Give the extent of all Plasmodium falciparum-infected red blood cells.
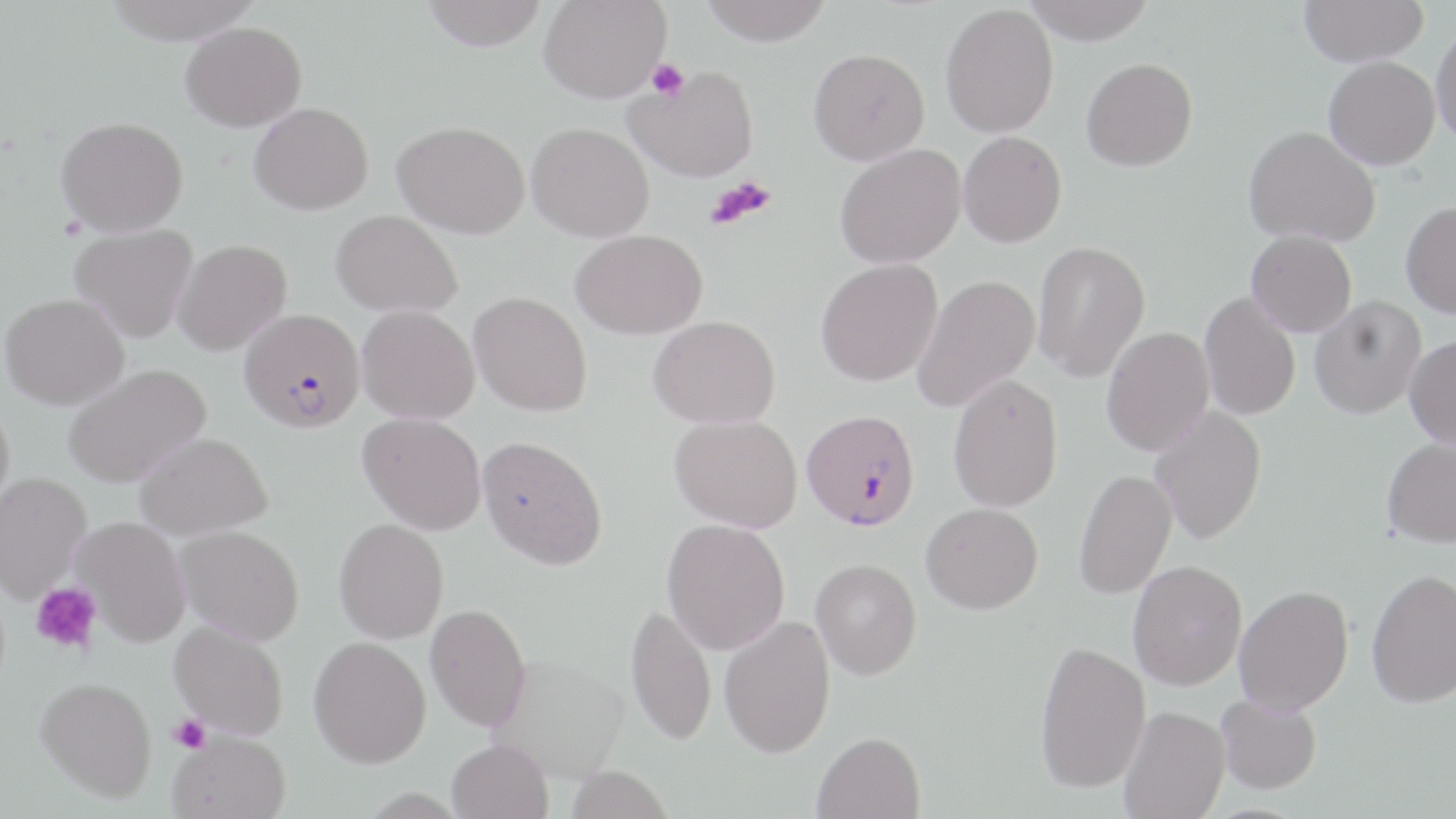

Approximate bounding boxes as named x1/y1/x2/y2 corners in pixels.
Plasmodium falciparum-infected red blood cells: (x1=239, y1=308, x2=366, y2=433), (x1=801, y1=408, x2=921, y2=531).

slide-level diagnosis = Plasmodium falciparum
preparation = thin blood film
magnification = 1000x
modality = optical microscopy
field of view = one of a larger specimen
stain = May-Grünwald-Giemsa
platelet locations = approximate bounding boxes as named x1/y1/x2/y2 corners in pixels: (x1=645, y1=59, x2=689, y2=100), (x1=707, y1=176, x2=777, y2=229), (x1=30, y1=582, x2=103, y2=655), (x1=168, y1=714, x2=211, y2=753)
image size = 1456×819 pixels
uninfected red blood cell locations = approximate bounding boxes as named x1/y1/x2/y2 corners in pixels: (x1=100, y1=0, x2=265, y2=44), (x1=420, y1=0, x2=549, y2=51), (x1=539, y1=0, x2=671, y2=102), (x1=699, y1=0, x2=833, y2=46), (x1=1021, y1=0, x2=1157, y2=44), (x1=1298, y1=0, x2=1428, y2=66), (x1=940, y1=3, x2=1059, y2=138), (x1=181, y1=21, x2=306, y2=131), (x1=1431, y1=21, x2=1456, y2=147), (x1=808, y1=48, x2=930, y2=165), (x1=1323, y1=56, x2=1440, y2=170), (x1=1081, y1=58, x2=1197, y2=171), (x1=626, y1=66, x2=759, y2=182), (x1=249, y1=102, x2=373, y2=215), (x1=56, y1=116, x2=188, y2=236), (x1=392, y1=121, x2=530, y2=239), (x1=526, y1=123, x2=654, y2=242), (x1=1243, y1=125, x2=1380, y2=246), (x1=958, y1=131, x2=1067, y2=247), (x1=834, y1=143, x2=966, y2=269), (x1=1401, y1=201, x2=1456, y2=318), (x1=331, y1=210, x2=462, y2=316), (x1=69, y1=223, x2=199, y2=342), (x1=570, y1=229, x2=708, y2=339), (x1=1246, y1=230, x2=1357, y2=337), (x1=172, y1=239, x2=291, y2=355), (x1=1032, y1=239, x2=1151, y2=383), (x1=815, y1=258, x2=942, y2=387), (x1=912, y1=274, x2=1040, y2=413), (x1=468, y1=291, x2=592, y2=416), (x1=1199, y1=291, x2=1301, y2=421), (x1=1, y1=293, x2=129, y2=410), (x1=1310, y1=296, x2=1426, y2=419), (x1=357, y1=305, x2=479, y2=423), (x1=648, y1=315, x2=781, y2=428), (x1=1101, y1=326, x2=1215, y2=457), (x1=1403, y1=334, x2=1456, y2=449), (x1=62, y1=363, x2=211, y2=488), (x1=948, y1=373, x2=1063, y2=512), (x1=0, y1=397, x2=15, y2=520), (x1=1148, y1=405, x2=1267, y2=546), (x1=358, y1=412, x2=487, y2=535), (x1=669, y1=414, x2=802, y2=532), (x1=134, y1=432, x2=273, y2=539), (x1=477, y1=434, x2=608, y2=570), (x1=1381, y1=435, x2=1456, y2=548), (x1=1073, y1=468, x2=1177, y2=600), (x1=0, y1=472, x2=90, y2=602), (x1=920, y1=503, x2=1043, y2=614), (x1=73, y1=516, x2=190, y2=646), (x1=333, y1=518, x2=448, y2=643), (x1=661, y1=518, x2=791, y2=654), (x1=175, y1=525, x2=304, y2=645), (x1=811, y1=559, x2=922, y2=680), (x1=1128, y1=560, x2=1247, y2=690), (x1=1366, y1=568, x2=1456, y2=707), (x1=1234, y1=585, x2=1353, y2=715), (x1=625, y1=601, x2=717, y2=746), (x1=426, y1=603, x2=531, y2=731), (x1=719, y1=616, x2=835, y2=758), (x1=170, y1=621, x2=289, y2=740), (x1=309, y1=635, x2=431, y2=768), (x1=1034, y1=639, x2=1150, y2=794), (x1=488, y1=654, x2=630, y2=780), (x1=36, y1=677, x2=157, y2=801), (x1=1216, y1=694, x2=1321, y2=794), (x1=1119, y1=706, x2=1230, y2=819), (x1=168, y1=729, x2=290, y2=819), (x1=813, y1=731, x2=925, y2=819), (x1=447, y1=739, x2=553, y2=819), (x1=564, y1=766, x2=675, y2=819)